Assess this cell for malaria.
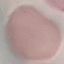
It is uninfected.

{
  "image_type": "automatically extracted cell patch, resized to 64 × 64 pixels",
  "preparation": "thin blood smear",
  "stain": "Giemsa",
  "capture": "smartphone camera at the microscope eyepiece"
}